Describe the morphology of the red blood cells.
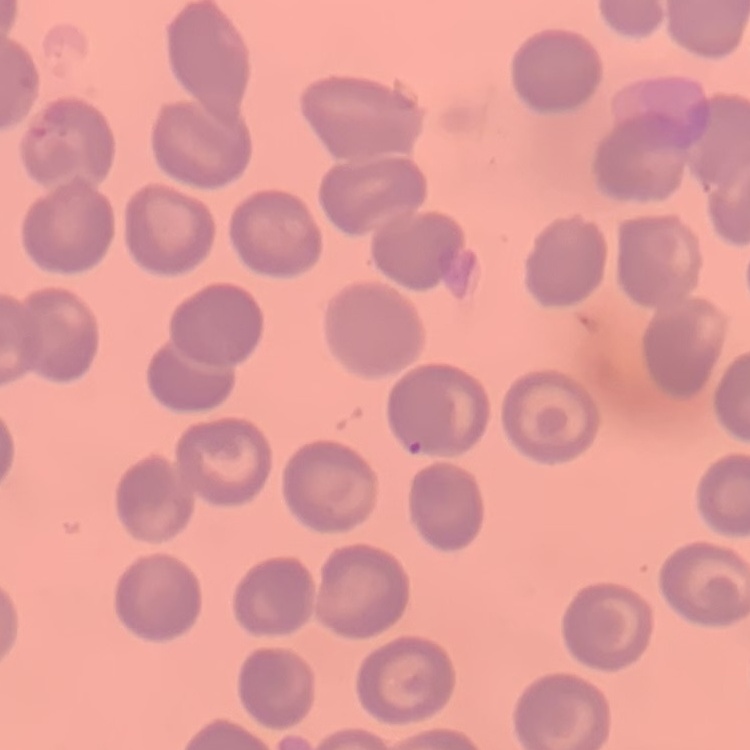

They show no rouleaux formation.

Summary:
  - Stain: Field's or Giemsa
  - Image type: one tile cut from a larger photomicrograph
  - Preparation: thin peripheral smear